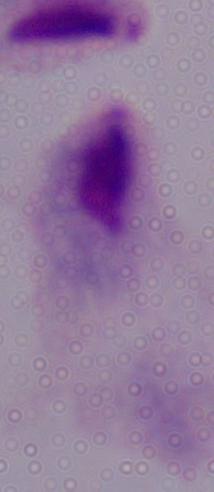

Summary:
  - Identification: trichomonad
  - Magnification: 1000x
  - Modality: micrograph